Outline each blood parasite and name the species.
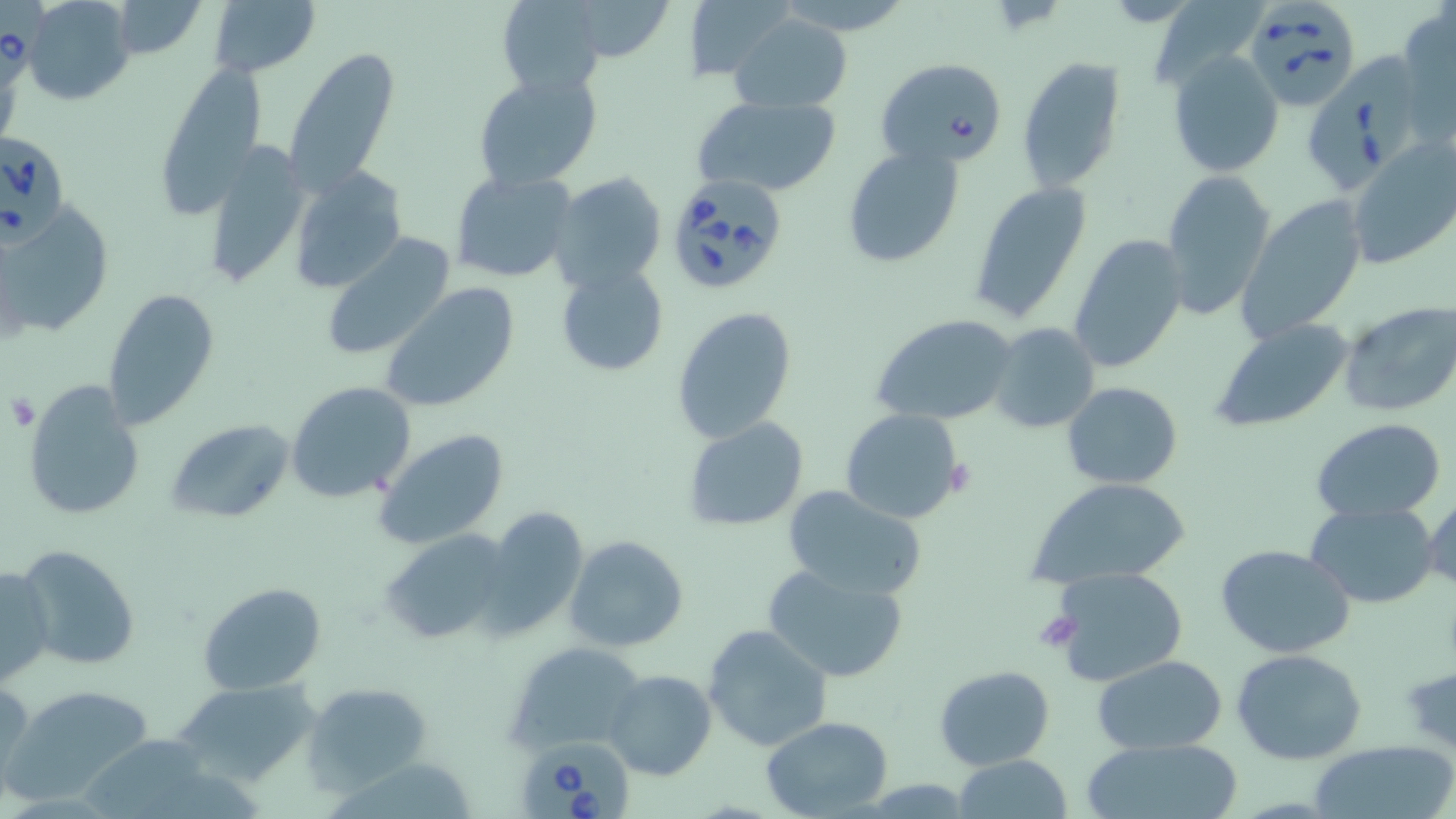
Approximate bounding boxes as (x1, y1, x2, y2) in pixels.
Babesia divergens-infected red blood cells: (1, 0, 45, 93), (1244, 1, 1362, 111), (1303, 49, 1419, 193), (875, 57, 1010, 169), (0, 129, 70, 243), (664, 174, 790, 295), (514, 736, 637, 819).
No Plasmodium falciparum, Plasmodium ovale, Plasmodium malariae, Plasmodium vivax, or Trypanosoma brucei observed.

{
  "slide_level_diagnosis": "Babesia divergens",
  "preparation": "thin blood smear",
  "uninfected_red_blood_cell_locations": "approximate bounding boxes as (x1, y1, x2, y2) in pixels: (22, 0, 136, 105), (111, 0, 208, 60), (208, 0, 320, 79), (497, 0, 608, 97), (573, 0, 675, 62), (684, 0, 797, 82), (1396, 6, 1456, 145), (728, 13, 853, 112), (284, 49, 401, 195), (1168, 51, 1284, 178), (1016, 56, 1128, 194), (153, 65, 264, 213), (473, 69, 602, 190), (691, 95, 842, 197), (201, 139, 310, 290), (1346, 139, 1456, 270), (841, 145, 965, 268), (289, 165, 406, 295), (1159, 168, 1277, 318), (449, 169, 579, 284), (549, 173, 667, 294), (968, 179, 1094, 325), (1236, 196, 1370, 346), (3, 206, 118, 343), (1065, 232, 1189, 374), (322, 233, 457, 361), (555, 263, 670, 376), (378, 282, 522, 414), (104, 288, 222, 429), (1338, 301, 1456, 419), (671, 306, 798, 444), (870, 313, 1020, 425), (1208, 318, 1356, 435), (988, 323, 1100, 434), (1061, 380, 1182, 490), (22, 381, 147, 522), (286, 381, 416, 503), (840, 408, 967, 527), (683, 417, 809, 532), (167, 418, 295, 523), (1311, 418, 1446, 523), (373, 427, 511, 550), (1027, 477, 1193, 589), (783, 485, 926, 599), (1423, 492, 1455, 596), (1306, 502, 1439, 607), (479, 508, 589, 638), (381, 529, 516, 647), (564, 536, 690, 654), (14, 544, 142, 673), (1215, 544, 1357, 659), (761, 561, 912, 683), (0, 564, 53, 687), (1046, 566, 1192, 687), (196, 579, 328, 694), (703, 624, 833, 753), (507, 641, 649, 753), (1231, 648, 1368, 765), (1092, 657, 1228, 753), (934, 665, 1056, 769), (604, 668, 717, 780), (0, 677, 34, 795), (169, 681, 321, 790), (303, 681, 434, 790), (6, 683, 159, 803), (761, 715, 894, 817), (1079, 737, 1244, 819), (1303, 742, 1455, 819), (951, 756, 1076, 817)",
  "stain": "May-Grünwald-Giemsa",
  "field_of_view": "one of a larger specimen",
  "magnification": "1000x",
  "platelet_locations": "approximate bounding boxes as (x1, y1, x2, y2) in pixels: (4, 393, 40, 432), (1033, 609, 1082, 651)",
  "image_size": "1456×819 pixels",
  "modality": "optical microscopy"
}